Point out each Plasmodium parasite.
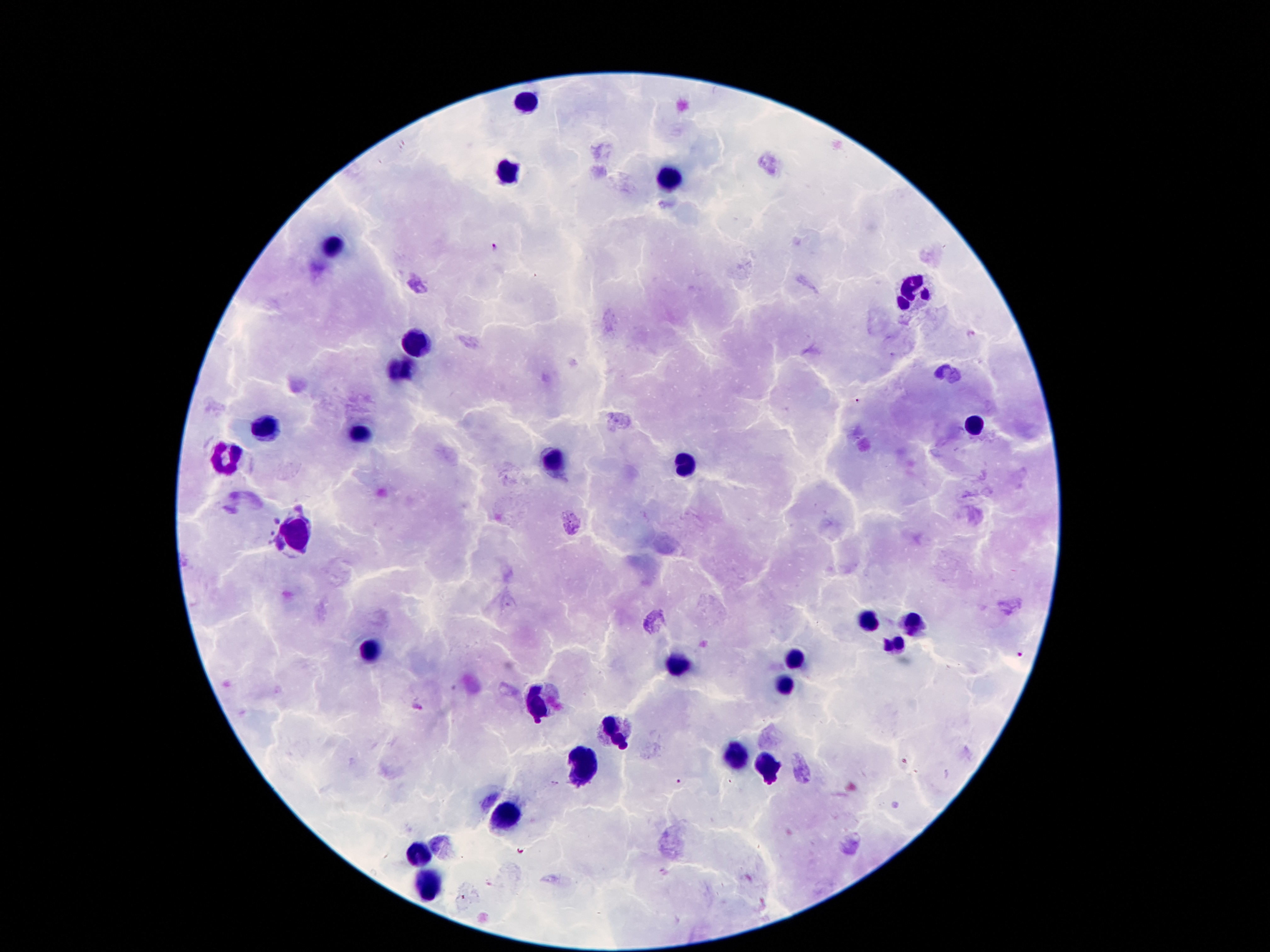
Approximate centers as [x, y] in pixels.
Plasmodium parasites: [497, 247], [970, 335], [1020, 656], [418, 707], [907, 762], [678, 781].

Leukocyte locations: [528, 102], [507, 171], [673, 177], [335, 246], [917, 288], [417, 343], [402, 373], [270, 425], [975, 425], [356, 435], [230, 457], [551, 459], [686, 463], [297, 532], [870, 618], [914, 620], [894, 643], [369, 652], [795, 660], [677, 667], [786, 685], [537, 700], [616, 729], [738, 755], [591, 765], [768, 765], [512, 814], [419, 855], [430, 885]. Patient malaria status: infected with Plasmodium falciparum. Image is 1270×952 pixels. 100x magnification. Thick peripheral-blood smear. Giemsa-stained preparation. Single field of view. Photographed through the microscope eyepiece with a smartphone camera.